Find the red blood cells that are infected with P. falciparum, and any of indeterminate infection status.
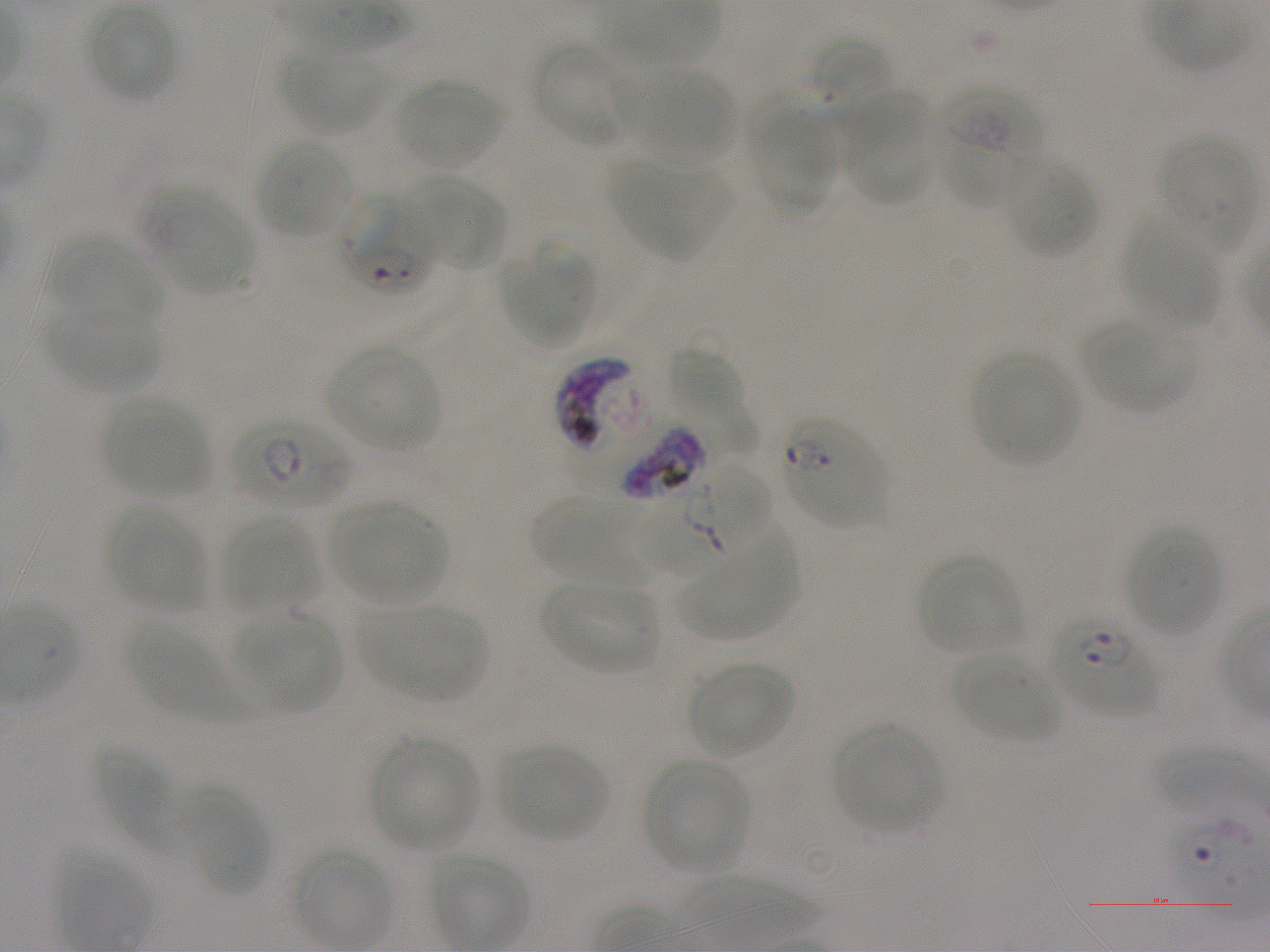

Approximate bounding rectangles given as corner coordinates in pixels from the top-left. Not every red blood cell is marked. A life-cycle stage — or a range of stages, where the recorded stages span more than one — follows each staged infected red blood cell.
Infected red blood cells: (x1=339, y1=197, x2=436, y2=294); (x1=232, y1=416, x2=351, y2=512) early ring to early trophozoite; (x1=782, y1=416, x2=887, y2=528); (x1=568, y1=418, x2=715, y2=502) late trophozoite to late schizont; (x1=642, y1=464, x2=772, y2=584) early ring to early trophozoite; (x1=1049, y1=612, x2=1158, y2=716) ring.
Red blood cells of indeterminate infection status: (x1=939, y1=83, x2=1038, y2=209), (x1=1158, y1=137, x2=1258, y2=251), (x1=555, y1=356, x2=643, y2=452).

Locations of uninfected red blood cells: (x1=87, y1=4, x2=177, y2=102), (x1=810, y1=37, x2=893, y2=120), (x1=532, y1=41, x2=633, y2=149), (x1=281, y1=51, x2=388, y2=136), (x1=623, y1=67, x2=734, y2=167), (x1=394, y1=78, x2=504, y2=171), (x1=745, y1=89, x2=837, y2=215), (x1=842, y1=94, x2=937, y2=205), (x1=257, y1=139, x2=354, y2=240), (x1=1003, y1=156, x2=1098, y2=258), (x1=608, y1=159, x2=730, y2=259), (x1=406, y1=177, x2=505, y2=273), (x1=142, y1=192, x2=259, y2=299), (x1=1125, y1=217, x2=1219, y2=328), (x1=48, y1=237, x2=163, y2=327), (x1=502, y1=244, x2=593, y2=349), (x1=45, y1=302, x2=161, y2=396), (x1=1085, y1=319, x2=1196, y2=414), (x1=666, y1=344, x2=760, y2=458), (x1=327, y1=346, x2=443, y2=451), (x1=971, y1=351, x2=1080, y2=466), (x1=100, y1=395, x2=212, y2=500), (x1=531, y1=496, x2=656, y2=585), (x1=329, y1=500, x2=448, y2=604), (x1=106, y1=505, x2=207, y2=613), (x1=220, y1=515, x2=319, y2=613), (x1=672, y1=519, x2=800, y2=640), (x1=1125, y1=525, x2=1224, y2=638), (x1=919, y1=554, x2=1023, y2=656), (x1=538, y1=580, x2=660, y2=676), (x1=360, y1=603, x2=488, y2=703), (x1=238, y1=612, x2=341, y2=713), (x1=129, y1=621, x2=240, y2=722), (x1=952, y1=653, x2=1062, y2=743), (x1=688, y1=662, x2=793, y2=758), (x1=833, y1=723, x2=945, y2=835), (x1=370, y1=737, x2=480, y2=851), (x1=498, y1=745, x2=608, y2=841), (x1=95, y1=748, x2=184, y2=853), (x1=644, y1=759, x2=751, y2=874), (x1=177, y1=788, x2=267, y2=894), (x1=291, y1=846, x2=394, y2=949), (x1=428, y1=853, x2=530, y2=950). Single field of view. Image is 1270×952 pixels. Blood group of the donor: A+. Thin blood film. 100x objective under oil immersion, numerical aperture 1.25. Giemsa-stained preparation. P. falciparum strain NF54 in static in-vitro culture.